Give the position of every malaria parasite, noting whether each is a trophozoite, schizont, or gametocyte.
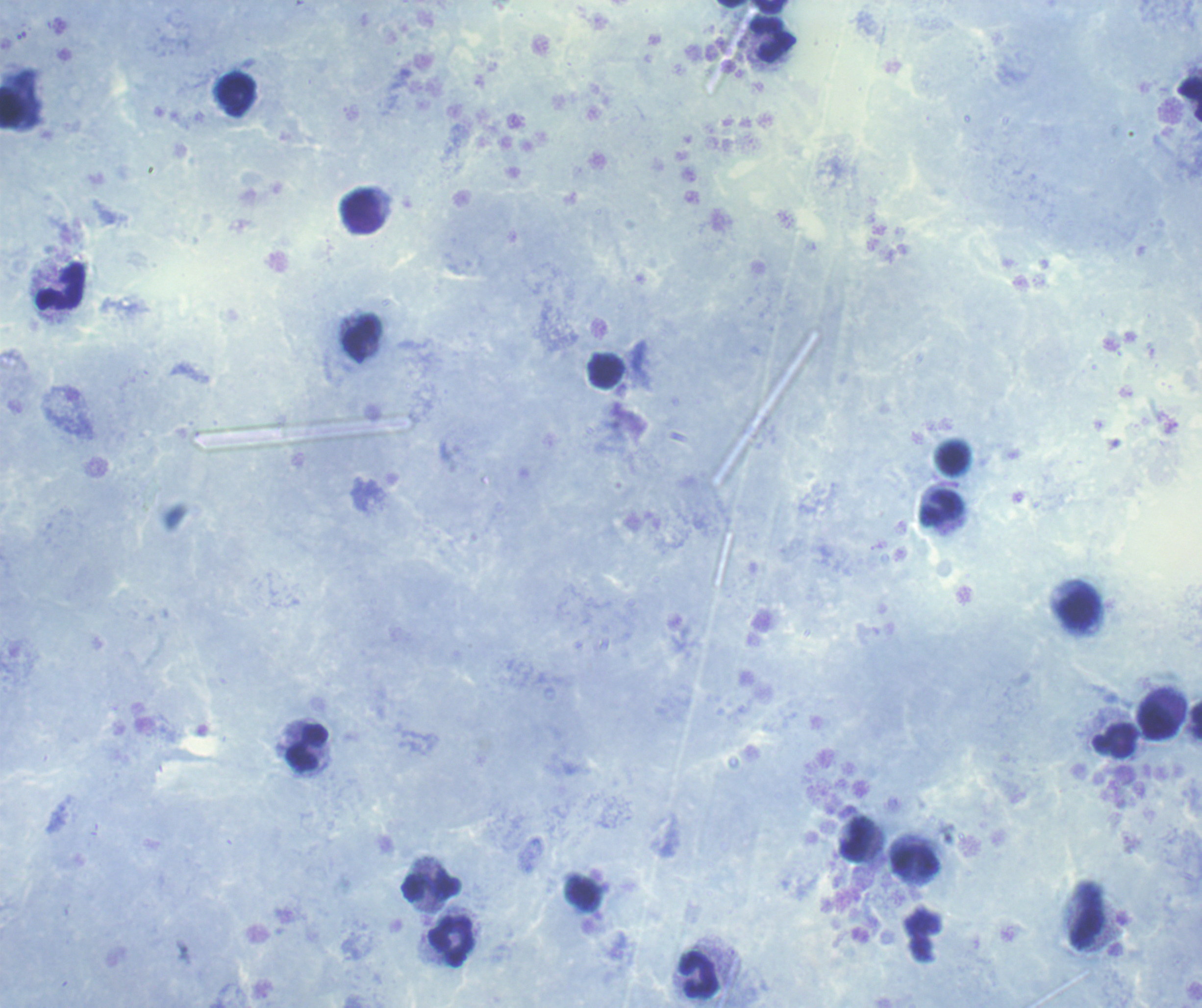

No malaria parasites seen.

Approximate centers as {x, y} in pixels. Leukocyte locations: {770, 7}, {774, 40}, {235, 96}, {1190, 98}, {363, 212}, {61, 287}, {363, 337}, {606, 371}, {952, 457}, {942, 507}, {1079, 608}, {1157, 722}, {1116, 740}, {308, 748}, {857, 838}, {917, 861}, {431, 885}, {1087, 915}, {452, 942}, {698, 975}. Coloration quality: good. Image is 1202×1008 pixels. Captured at 100x magnification. Thick blood smear. One field from this slide. Previously used in an actual diagnosis. Background quality: good. Romanowsky stain.